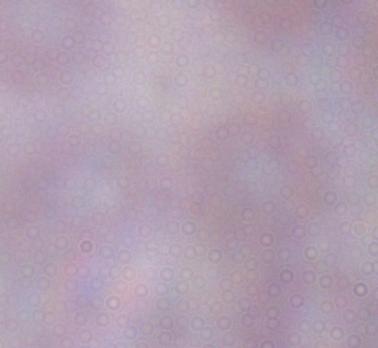
1000x magnification. Photomicrograph. A trypanosome is seen.